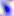
Summary:
  - Identification: Toxoplasma gondii
  - Modality: micrograph
  - Magnification: 400x